Identify the parasite.
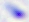

Toxoplasma gondii.

Micrograph. 400x magnification.